Classify this cell by malaria status.
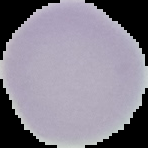

It is uninfected.

image type = cell region segmented out of the field of view; surrounding area masked to black
image size = 148×148 pixels
preparation = thin blood film